Classify this cell by malaria status.
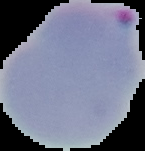

Parasitized.

Summary:
  - Image size: 145×151 pixels
  - Preparation: thin blood smear
  - Image type: segmented cell region with the area outside set to black